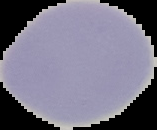
Image is 157×130 pixels. Malaria status: uninfected. From a thin blood smear. Cell region segmented out of the field of view; the surrounding area is masked to black.